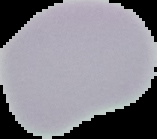

From a thin blood film. Malaria status: uninfected. Image is 157×139 pixels. The area outside the segmented cell region is set to black.